Name the parasite shown.
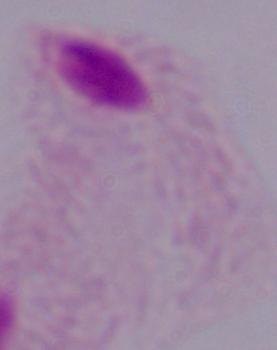

A trichomonad.

modality = photomicrograph
magnification = 1000x